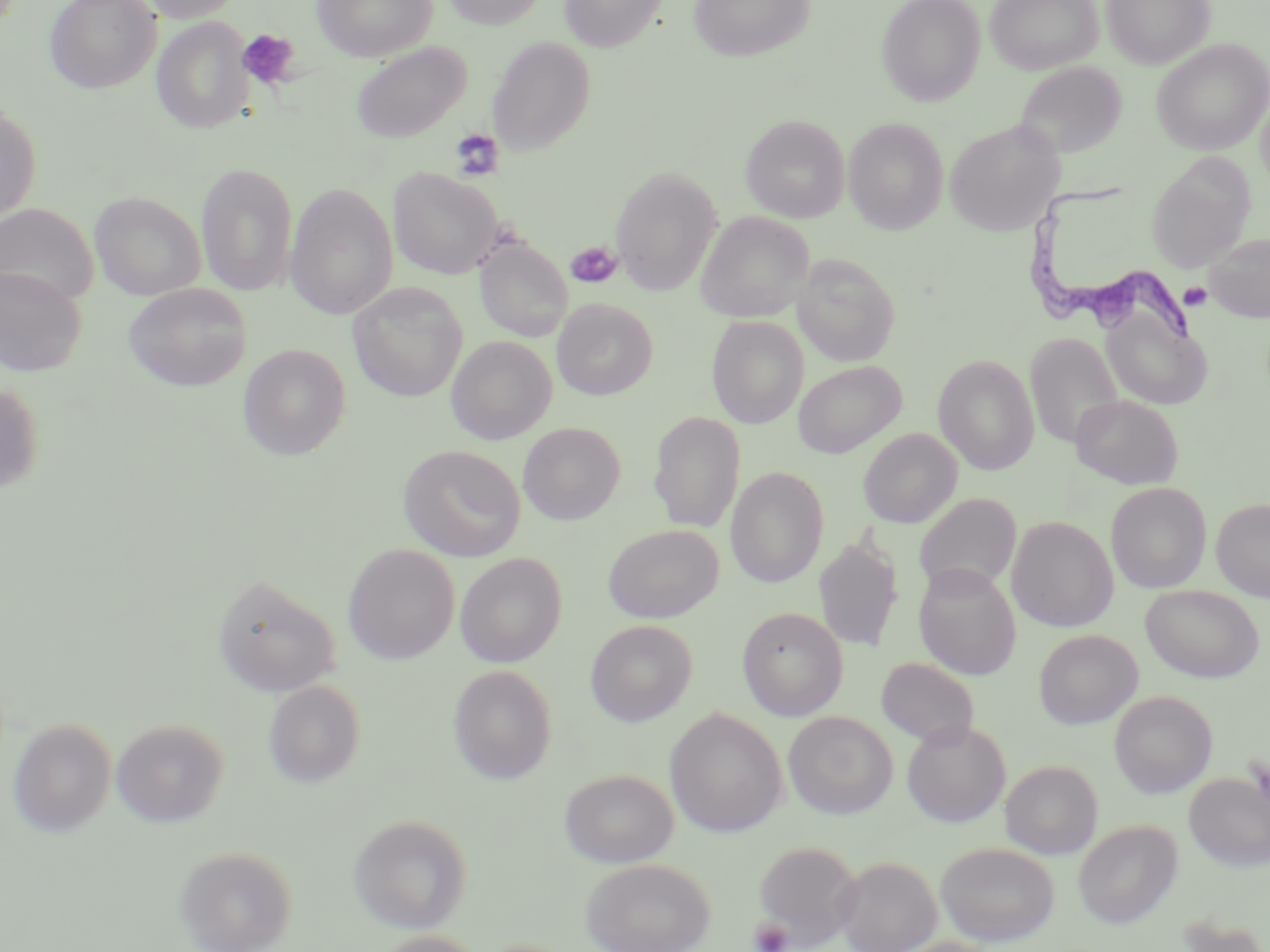
Approximate bounding boxes as [x1, y1, x2, y2] in pixels. Platelet locations: [237, 28, 300, 90], [449, 127, 504, 180], [566, 240, 624, 288], [1179, 282, 1213, 311], [749, 917, 793, 951]. Trypanosoma brucei locations: [1021, 181, 1196, 345]. Uninfected red blood cell locations: [130, 0, 246, 22], [313, 0, 437, 62], [441, 0, 546, 29], [558, 0, 668, 52], [687, 0, 816, 62], [877, 0, 985, 106], [985, 0, 1102, 74], [1101, 0, 1214, 69], [45, 1, 160, 94], [152, 17, 254, 133], [487, 36, 595, 156], [1151, 39, 1270, 155], [352, 42, 472, 142], [1014, 62, 1127, 160], [1256, 96, 1270, 193], [0, 100, 41, 227], [741, 115, 850, 223], [843, 117, 949, 234], [945, 120, 1063, 236], [1146, 154, 1255, 273], [195, 162, 298, 297], [610, 165, 723, 295], [386, 166, 505, 280], [286, 182, 398, 320], [89, 191, 205, 300], [0, 202, 98, 306], [696, 212, 814, 322], [1204, 233, 1270, 322], [475, 237, 572, 343], [792, 255, 900, 366], [0, 266, 86, 376], [123, 282, 251, 391], [348, 283, 467, 402], [553, 298, 657, 400], [1102, 310, 1213, 410], [706, 315, 808, 428], [1024, 332, 1123, 450], [446, 335, 556, 444], [238, 344, 351, 460], [933, 354, 1039, 475], [793, 360, 906, 459], [0, 382, 43, 496], [1072, 394, 1183, 489], [648, 412, 745, 533], [518, 422, 624, 525], [858, 428, 962, 528], [397, 445, 527, 562], [725, 466, 829, 588], [1106, 482, 1211, 593], [914, 493, 1021, 597], [1211, 498, 1270, 602], [1007, 516, 1118, 632], [603, 524, 723, 623], [814, 536, 904, 651], [342, 544, 460, 664], [455, 552, 567, 668], [913, 564, 1021, 680], [212, 574, 341, 697], [1140, 584, 1264, 683], [736, 606, 848, 721], [585, 620, 697, 726], [1034, 629, 1142, 729], [876, 656, 980, 748], [448, 664, 557, 785], [263, 680, 365, 788], [1109, 690, 1217, 798], [665, 707, 788, 837], [783, 711, 898, 819], [8, 718, 116, 838], [111, 718, 229, 827], [902, 720, 1011, 828], [1001, 759, 1102, 859], [559, 768, 679, 867], [1184, 771, 1270, 871], [348, 814, 472, 933], [1073, 820, 1183, 929], [751, 838, 864, 947], [935, 842, 1060, 945], [173, 844, 299, 952], [833, 856, 942, 952], [580, 857, 716, 951], [1174, 914, 1268, 952], [368, 930, 487, 952], [890, 936, 1001, 952]. Slide-level diagnosis: Trypanosoma brucei. Light microscopy. Thin blood film. Image is 1270×952 pixels. One field of a larger specimen. May-Grünwald-Giemsa stain. Captured at 1000x magnification.